Identify the cell.
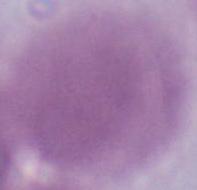
This is an erythrocyte.

Micrograph. 1000x magnification.